Name the parasite shown.
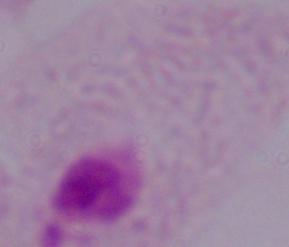

A trichomonad.

magnification = 1000x
modality = photomicrograph